Give the position of every P. falciparum parasite, noting its life-cycle stage.
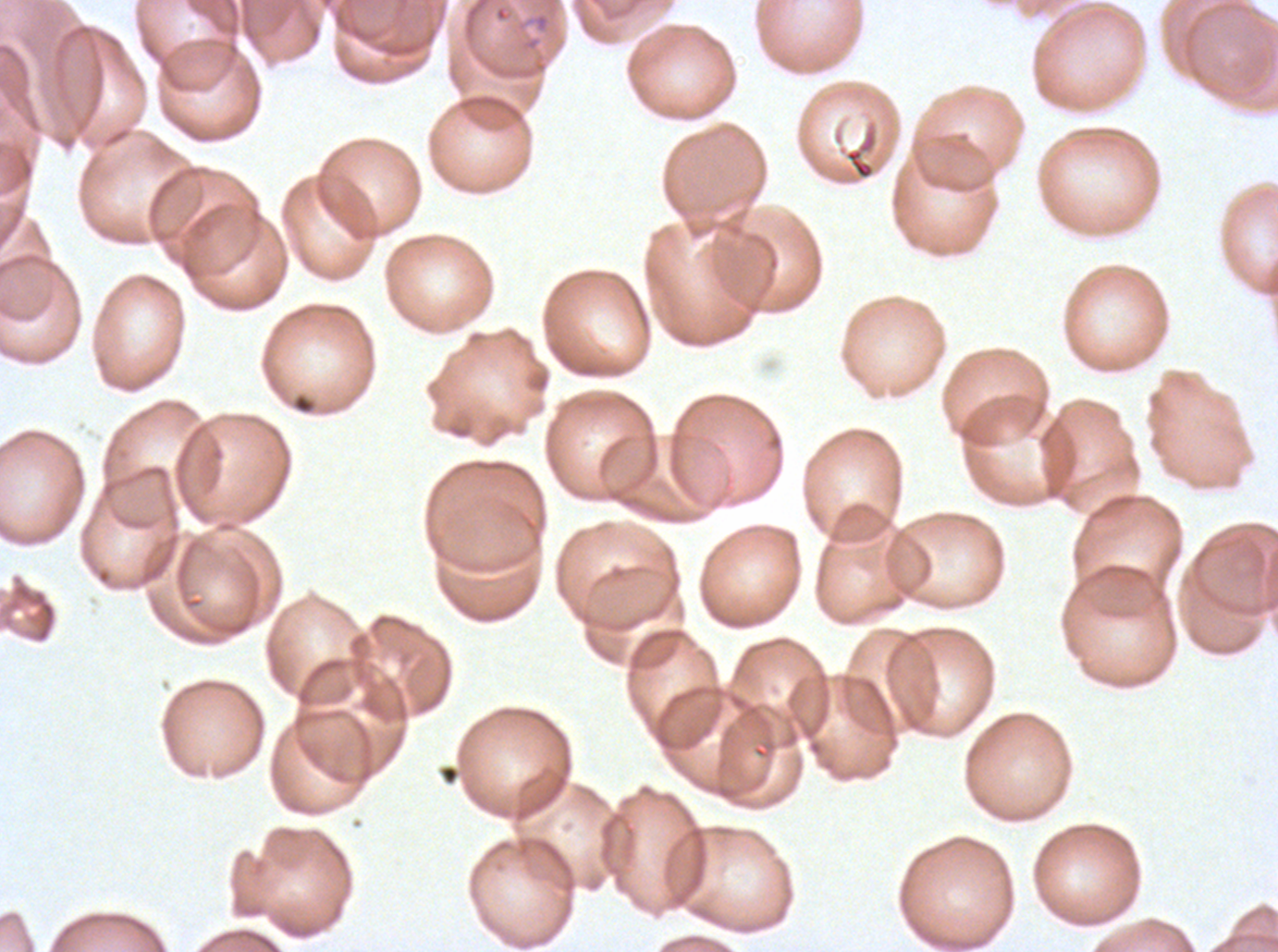

No rings, late-ring/early-trophozoite forms, mid trophozoites, late trophozoites, early schizonts, late schizonts, segmenters, or gametocytes observed.

preparation: thin blood film
stain: Giemsa
field_of_view: sub-image separated from a larger composite
debris_locations: 'approximate bounding boxes as [x1, y1, x2, y2] in pixels: [291, 392, 316, 415], [438, 763, 461, 786]'
specimen: P. falciparum cultured ex vivo for 24 to 48 hours, from a patient in The Gambia
image_size: 1278×952 pixels